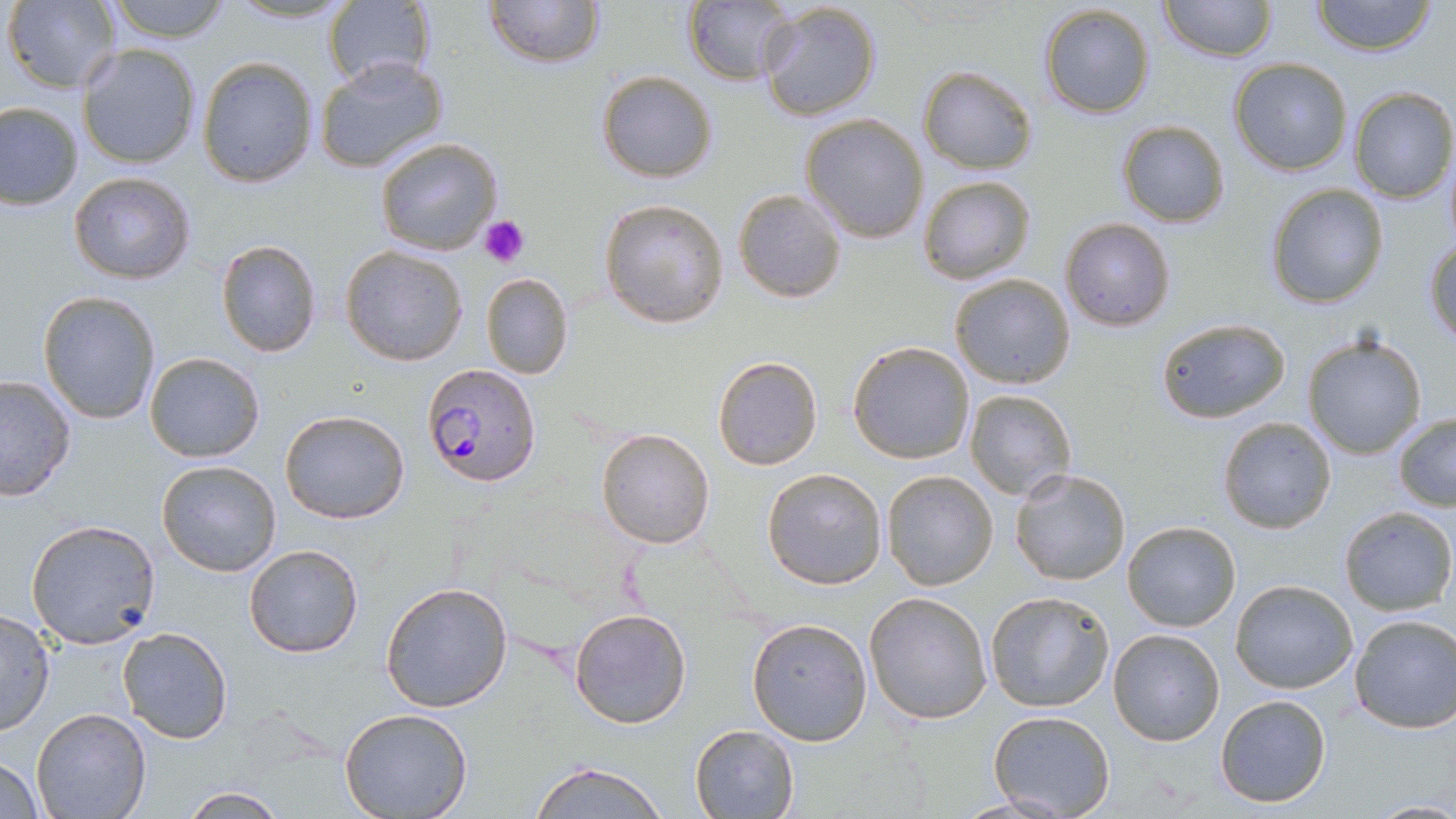
Summary:
  - Coordinate format: approximate bounding boxes as named x1/y1/x2/y2 corners in pixels
  - Platelet locations: (x1=478, y1=214, x2=531, y2=267)
  - Uninfected red blood cell locations: (x1=225, y1=0, x2=357, y2=25), (x1=324, y1=0, x2=433, y2=92), (x1=484, y1=0, x2=604, y2=68), (x1=1158, y1=0, x2=1274, y2=62), (x1=1311, y1=0, x2=1438, y2=56), (x1=5, y1=1, x2=122, y2=93), (x1=102, y1=1, x2=235, y2=44), (x1=683, y1=2, x2=797, y2=85), (x1=1038, y1=3, x2=1156, y2=119), (x1=758, y1=4, x2=882, y2=122), (x1=77, y1=45, x2=202, y2=169), (x1=197, y1=56, x2=318, y2=187), (x1=314, y1=57, x2=450, y2=174), (x1=1228, y1=58, x2=1352, y2=175), (x1=918, y1=65, x2=1037, y2=173), (x1=596, y1=70, x2=718, y2=183), (x1=1347, y1=87, x2=1456, y2=203), (x1=0, y1=102, x2=83, y2=210), (x1=800, y1=113, x2=930, y2=242), (x1=1116, y1=119, x2=1230, y2=227), (x1=375, y1=136, x2=503, y2=256), (x1=1442, y1=146, x2=1456, y2=248), (x1=69, y1=171, x2=196, y2=284), (x1=917, y1=175, x2=1035, y2=284), (x1=1265, y1=183, x2=1389, y2=309), (x1=733, y1=188, x2=847, y2=303), (x1=598, y1=199, x2=730, y2=329), (x1=1060, y1=217, x2=1175, y2=331), (x1=1424, y1=236, x2=1456, y2=345), (x1=215, y1=240, x2=322, y2=357), (x1=341, y1=245, x2=469, y2=366), (x1=480, y1=272, x2=573, y2=379), (x1=948, y1=274, x2=1076, y2=389), (x1=38, y1=291, x2=162, y2=426), (x1=1155, y1=318, x2=1292, y2=422), (x1=1302, y1=331, x2=1428, y2=461), (x1=847, y1=341, x2=975, y2=464), (x1=144, y1=352, x2=265, y2=463), (x1=711, y1=354, x2=824, y2=470), (x1=0, y1=373, x2=79, y2=503), (x1=963, y1=388, x2=1076, y2=500), (x1=280, y1=409, x2=409, y2=525), (x1=1393, y1=412, x2=1456, y2=512), (x1=1217, y1=416, x2=1337, y2=535), (x1=595, y1=427, x2=715, y2=549), (x1=156, y1=460, x2=282, y2=578), (x1=761, y1=467, x2=889, y2=589), (x1=1009, y1=467, x2=1131, y2=586), (x1=881, y1=470, x2=999, y2=591), (x1=1337, y1=505, x2=1455, y2=615), (x1=27, y1=519, x2=161, y2=648), (x1=1123, y1=520, x2=1240, y2=632), (x1=244, y1=543, x2=364, y2=658), (x1=1230, y1=579, x2=1358, y2=693), (x1=380, y1=581, x2=513, y2=715), (x1=863, y1=590, x2=994, y2=724), (x1=985, y1=590, x2=1115, y2=712), (x1=569, y1=608, x2=693, y2=729), (x1=0, y1=609, x2=55, y2=736), (x1=1349, y1=614, x2=1455, y2=736), (x1=746, y1=617, x2=872, y2=745), (x1=116, y1=626, x2=233, y2=744), (x1=1107, y1=628, x2=1225, y2=747), (x1=1213, y1=693, x2=1332, y2=809), (x1=339, y1=708, x2=474, y2=819), (x1=31, y1=709, x2=153, y2=819), (x1=987, y1=710, x2=1115, y2=818), (x1=690, y1=724, x2=798, y2=818), (x1=0, y1=754, x2=46, y2=818), (x1=528, y1=761, x2=671, y2=819), (x1=180, y1=786, x2=288, y2=817), (x1=1367, y1=799, x2=1456, y2=817)
  - Plasmodium falciparum-infected red blood cell locations: (x1=424, y1=362, x2=541, y2=487)
  - Slide-level diagnosis: Plasmodium falciparum
  - Stain: May-Grünwald-Giemsa
  - Preparation: thin blood film
  - Modality: optical microscopy
  - Image size: 1456×819 pixels
  - Magnification: 1000x
  - Field of view: single